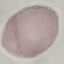
Result: no malaria parasites detected. Cell patch, automatically extracted from a larger field of view and resized to 64 × 64 pixels. Thin blood smear. Acquired by smartphone through the microscope eyepiece. Giemsa-stained preparation.